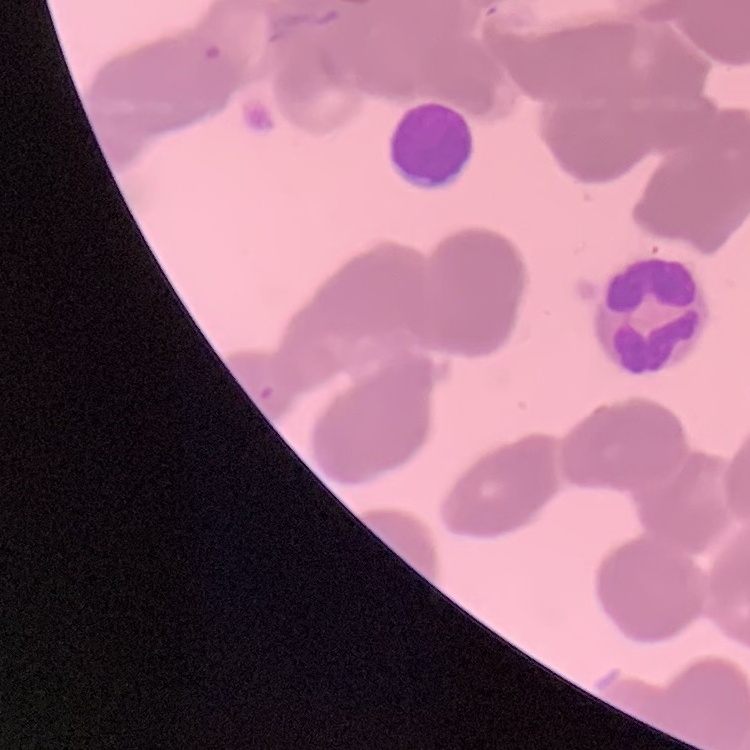

The red blood cells show rouleaux formation. Stained with either Field's or Giemsa. One tile cut from a larger photomicrograph. Thin blood smear.